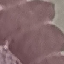
Malaria status: uninfected. Giemsa-stained preparation. Photographed with a smartphone camera at the microscope eyepiece. Thin blood smear. Automatically extracted cell patch, resized to 64 × 64 pixels.